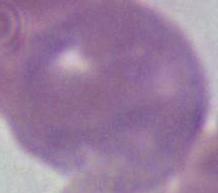

An erythrocyte is seen. Captured at 1000x magnification. Micrograph.